Locate every blood parasite and identify its species.
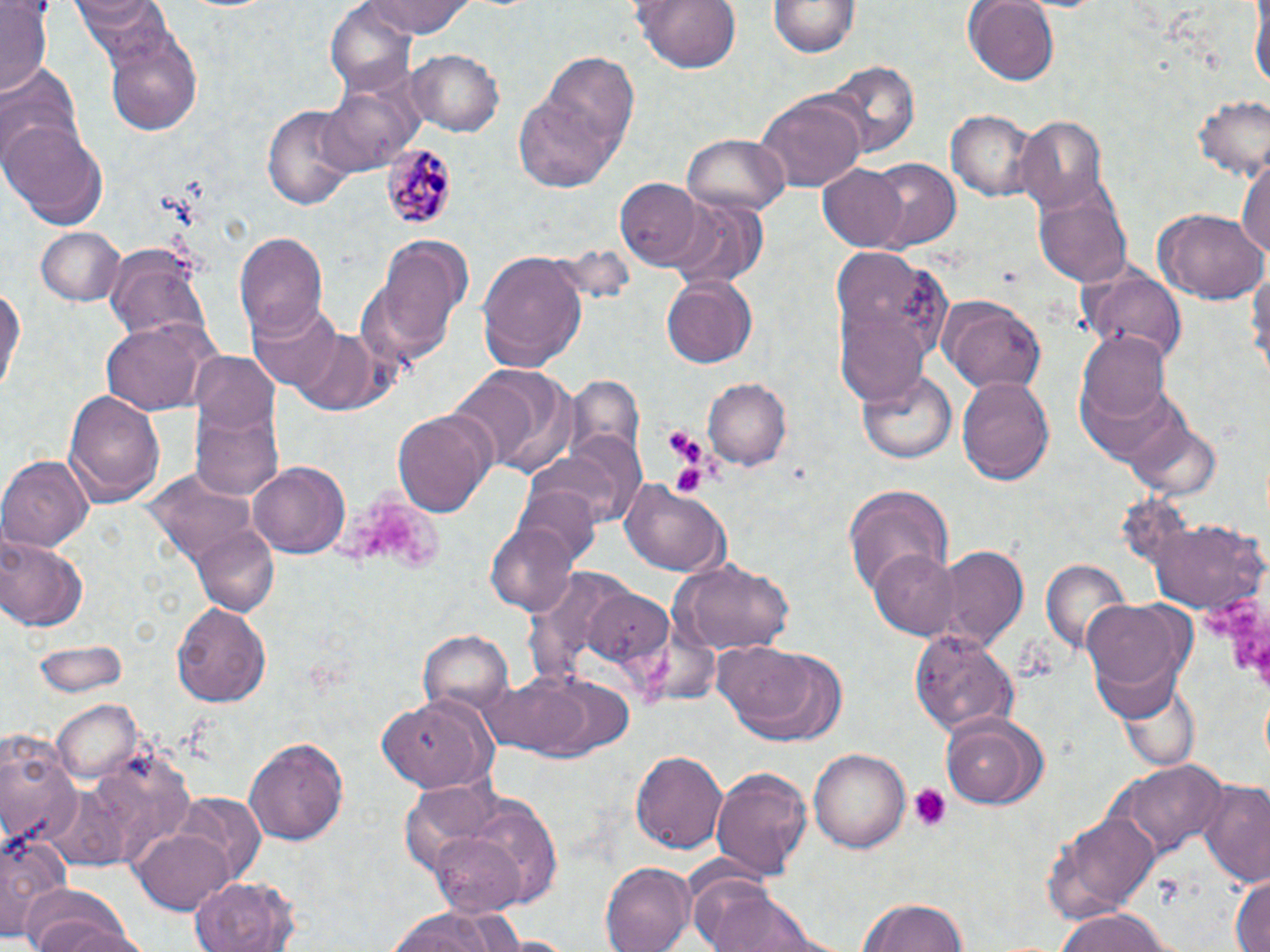

Approximate bounding boxes as (x1,y1)-(x2,y2) corner pairs in pixels.
Plasmodium malariae-infected red blood cells: (380,142)-(455,230).
No Plasmodium falciparum, Plasmodium ovale, Plasmodium vivax, Babesia divergens, or Trypanosoma brucei observed.

Uninfected red blood cell locations: (0,0)-(51,93), (355,0)-(483,37), (630,0)-(746,73), (964,0)-(1059,85), (1252,0)-(1268,98), (71,1)-(171,48), (771,1)-(858,57), (326,4)-(416,94), (102,30)-(204,137), (407,48)-(503,136), (522,57)-(639,190), (819,61)-(919,160), (0,68)-(84,170), (321,77)-(422,174), (1193,93)-(1269,180), (757,94)-(864,190), (261,103)-(360,211), (945,110)-(1035,201), (1014,115)-(1114,214), (2,118)-(109,227), (684,134)-(789,215), (1236,151)-(1270,263), (863,157)-(961,251), (818,164)-(909,252), (615,179)-(702,266), (1033,181)-(1132,290), (669,201)-(766,288), (1156,208)-(1265,304), (36,227)-(126,306), (232,229)-(328,338), (373,235)-(471,357), (104,241)-(211,348), (831,246)-(949,376), (477,250)-(589,371), (1248,256)-(1270,381), (1079,267)-(1188,362), (661,276)-(759,368), (0,277)-(24,402), (936,293)-(1048,393), (246,301)-(341,392), (833,309)-(931,406), (99,319)-(216,414), (290,326)-(385,414), (1077,333)-(1171,423), (189,353)-(280,436), (451,364)-(580,478), (957,370)-(1055,482), (857,371)-(956,464), (705,378)-(791,468), (64,388)-(167,507), (191,406)-(283,502), (389,407)-(497,517), (523,446)-(633,532), (0,452)-(93,552), (249,461)-(350,558), (621,479)-(729,577), (842,485)-(953,596), (516,486)-(601,568), (1141,516)-(1267,614), (485,520)-(581,617), (191,523)-(280,617), (1,533)-(90,633), (932,547)-(1026,647), (868,548)-(960,638), (670,557)-(797,656), (1041,558)-(1135,659), (1082,596)-(1188,703), (172,601)-(272,707), (420,629)-(513,720), (905,629)-(1017,737), (33,639)-(129,697), (716,639)-(851,744), (479,673)-(635,763), (1115,676)-(1202,774), (373,694)-(498,790), (51,700)-(143,783), (939,711)-(1051,811), (0,729)-(82,851), (242,736)-(349,847), (809,746)-(910,853), (632,747)-(727,856), (1108,761)-(1225,860), (709,766)-(813,880), (1197,779)-(1270,887), (173,792)-(265,879), (1049,807)-(1162,918), (0,824)-(74,939), (134,826)-(233,913), (427,833)-(527,914), (599,863)-(695,952), (1228,872)-(1269,952), (192,873)-(300,951), (688,875)-(790,952), (17,886)-(142,952), (856,894)-(970,952), (712,895)-(828,952), (380,907)-(525,952), (1055,907)-(1177,952). Platelet locations: (664,424)-(704,464), (670,460)-(709,498), (342,487)-(450,572), (1206,592)-(1269,690), (908,783)-(953,830). Slide-level diagnosis: Plasmodium malariae. May-Grünwald-Giemsa-stained preparation. Thin blood film. Image is 1270×952 pixels. Light microscopy. Captured at 1000x magnification. Single field of view.